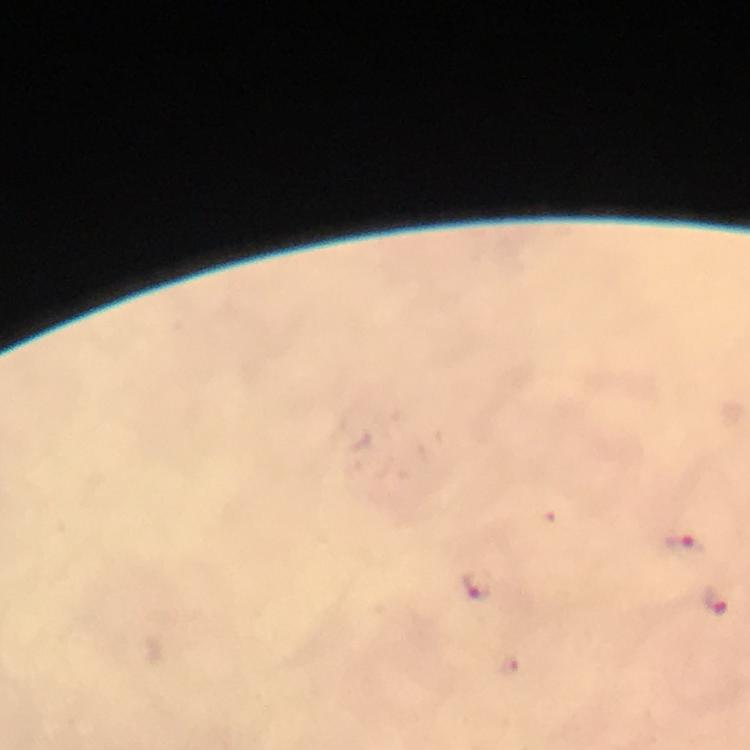

context = from a malaria diagnostic workup
immersion oil = used
magnification = 100x
preparation = thick blood smear
stain = Giemsa
cropped from = a single field of view
malaria parasite locations = approximate centers as {x, y} in pixels: {683, 547}, {476, 584}, {715, 600}, {509, 664}
capture = smartphone mounted on the microscope
image size = 750×750 pixels